Identify the parasite.
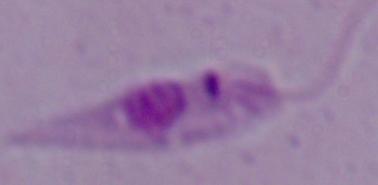

This is Leishmania.

Summary:
  - Modality: photomicrograph
  - Magnification: 1000x